Locate every Babesia divergens-infected red blood cell.
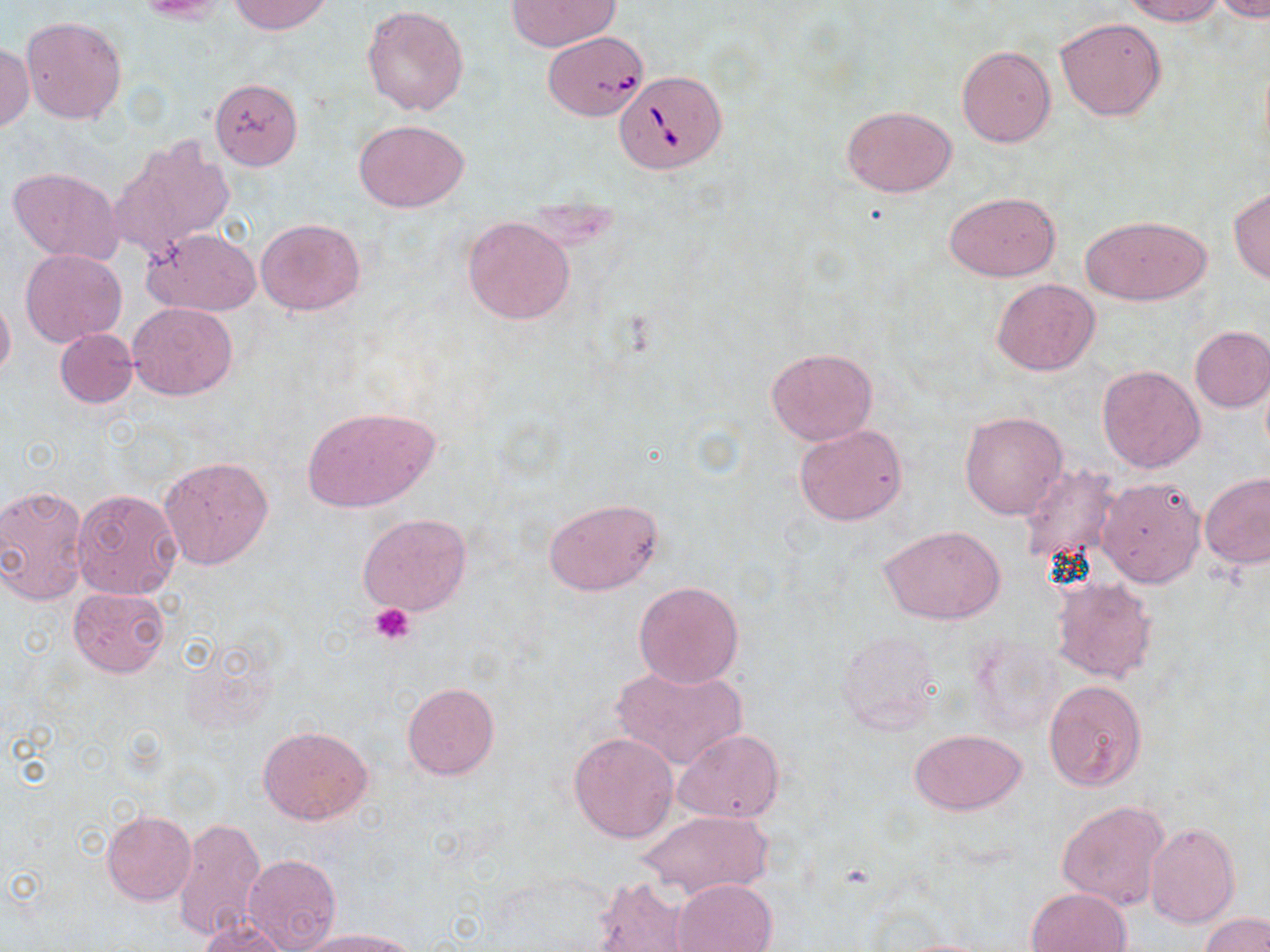
Approximate bounding boxes as [x1, y1, x2, y2] in pixels.
Babesia divergens-infected red blood cells: [538, 33, 650, 120], [615, 68, 726, 172].

slide_level_diagnosis: Babesia divergens
magnification: 1000x
uninfected_red_blood_cell_locations: 'approximate bounding boxes as [x1, y1, x2, y2] in pixels: [229, 0, 331, 34], [506, 0, 619, 51], [1123, 0, 1224, 25], [1213, 0, 1270, 21], [361, 3, 470, 116], [20, 15, 127, 124], [1055, 16, 1167, 121], [0, 43, 35, 131], [956, 45, 1055, 148], [210, 78, 303, 170], [842, 106, 955, 198], [354, 117, 471, 213], [110, 134, 236, 257], [7, 167, 124, 264], [1229, 188, 1270, 283], [946, 191, 1061, 281], [1080, 214, 1211, 305], [462, 216, 574, 324], [255, 218, 367, 314], [144, 227, 262, 316], [20, 249, 127, 345], [992, 278, 1100, 376], [0, 291, 16, 384], [128, 302, 238, 401], [1189, 326, 1270, 412], [55, 329, 138, 408], [765, 346, 878, 444], [1097, 364, 1205, 472], [775, 376, 897, 500], [301, 406, 439, 512], [960, 410, 1068, 520], [793, 423, 908, 526], [158, 456, 274, 570], [1018, 463, 1124, 570], [1201, 472, 1270, 568], [1097, 475, 1205, 587], [0, 484, 89, 608], [71, 488, 183, 600], [542, 496, 665, 597], [357, 513, 472, 618], [879, 524, 1007, 625], [1052, 577, 1157, 682], [633, 581, 745, 688], [68, 587, 170, 678], [836, 628, 944, 735], [966, 632, 1064, 740], [611, 664, 747, 771], [1044, 679, 1148, 793], [402, 682, 500, 780], [258, 724, 372, 825], [673, 728, 784, 824], [911, 729, 1026, 815], [568, 732, 680, 843], [1056, 800, 1169, 910], [637, 809, 773, 899], [102, 810, 195, 906], [170, 816, 266, 946], [1144, 823, 1241, 928], [243, 853, 341, 952], [593, 876, 695, 952], [670, 879, 777, 951], [1025, 887, 1133, 951], [1201, 913, 1269, 951], [197, 916, 291, 952], [299, 928, 418, 952], [880, 936, 1006, 951]'
stain: May-Grünwald-Giemsa
platelet_locations: 'approximate bounding boxes as [x1, y1, x2, y2] in pixels: [368, 602, 415, 644]'
image_size: 1270×952 pixels
preparation: thin blood film
modality: optical microscopy
field_of_view: one of a larger specimen